Classify this cell by malaria status.
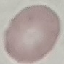

It is uninfected.

capture: smartphone through the microscope eyepiece
stain: Giemsa
image_type: automatically extracted cell patch, resized to 64 × 64 pixels
preparation: thin blood smear